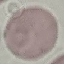
malaria status = uninfected
capture = smartphone camera at the microscope eyepiece
stain = Giemsa
image type = automatically extracted cell patch, resized to 64 × 64 pixels
preparation = thin blood film